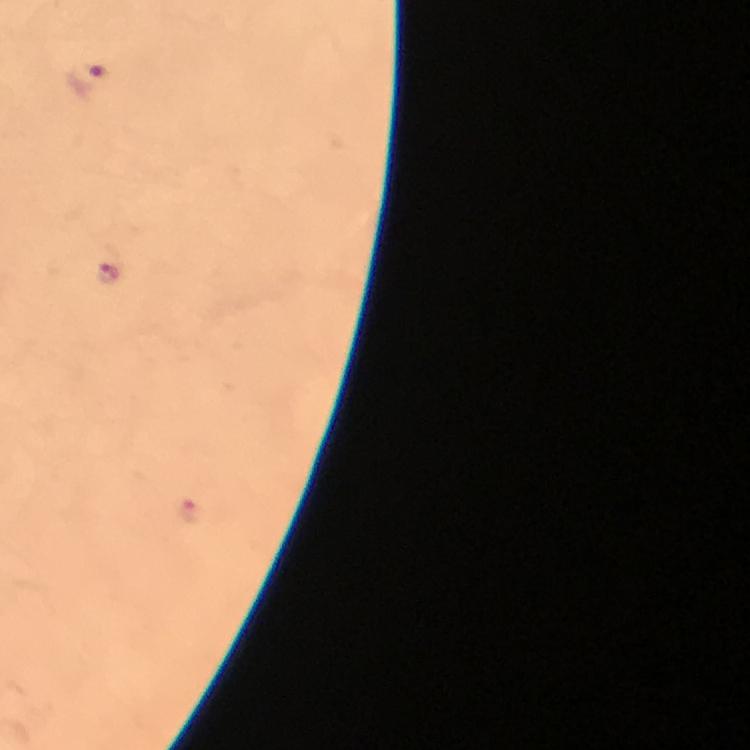

Approximate centers as [x, y] in pixels.
Summary:
  - Malaria parasite locations: [88, 79], [109, 274], [194, 510]
  - Immersion oil: applied
  - Magnification: 100x
  - Preparation: thick blood film
  - Context: from a malaria diagnostic workup
  - Capture: smartphone camera through the microscope
  - Image size: 750×750 pixels
  - Stain: Giemsa
  - Cropped from: one field of view